Give the extent of all uninfected red blood cells.
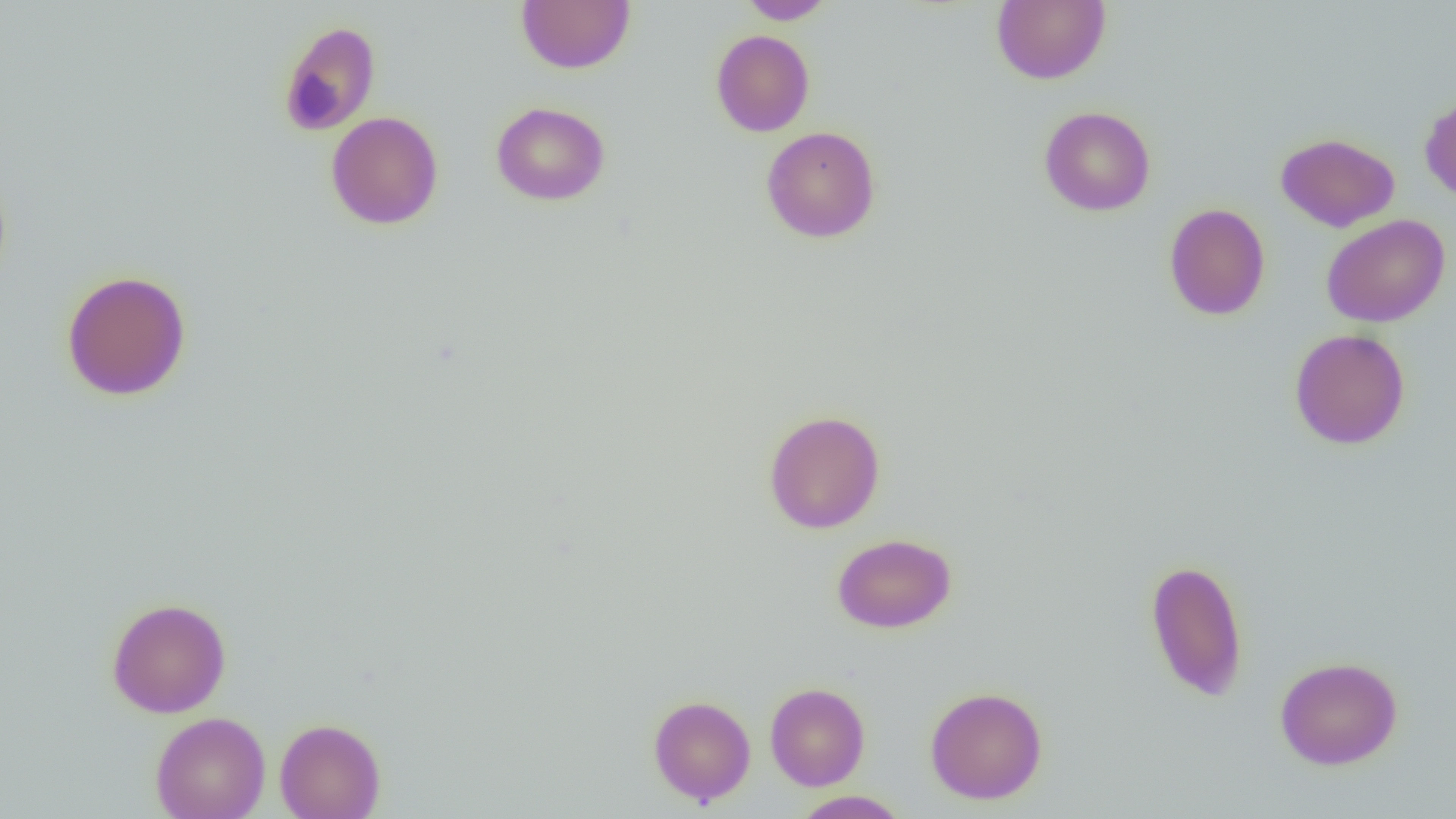
Approximate bounding boxes as (x1, y1, x2, y2) in pixels.
Uninfected red blood cells: (736, 0, 836, 24), (992, 0, 1111, 85), (517, 1, 635, 74), (278, 20, 381, 136), (711, 30, 815, 137), (1419, 93, 1456, 203), (491, 101, 610, 206), (1039, 106, 1156, 216), (326, 111, 444, 230), (761, 125, 880, 243), (1275, 132, 1400, 232), (1164, 203, 1270, 320), (1321, 213, 1450, 328), (61, 270, 192, 401), (1288, 328, 1411, 450), (763, 409, 886, 534), (832, 533, 957, 634), (1144, 558, 1249, 702), (106, 597, 232, 718), (1274, 656, 1403, 770), (765, 682, 870, 790), (924, 685, 1048, 805), (648, 694, 756, 805), (150, 711, 271, 819), (274, 717, 386, 819), (791, 790, 911, 818).

Summary:
  - Slide-level diagnosis: no evidence of blood parasites
  - Magnification: 1000x
  - Preparation: thin blood smear
  - Modality: optical microscopy
  - Field of view: one of a larger specimen
  - Image size: 1456×819 pixels